Classify this cell by malaria status.
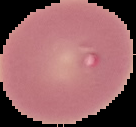

It is uninfected.

Image is 136×127 pixels. The area outside the segmented cell region is set to black. From a thin blood film.